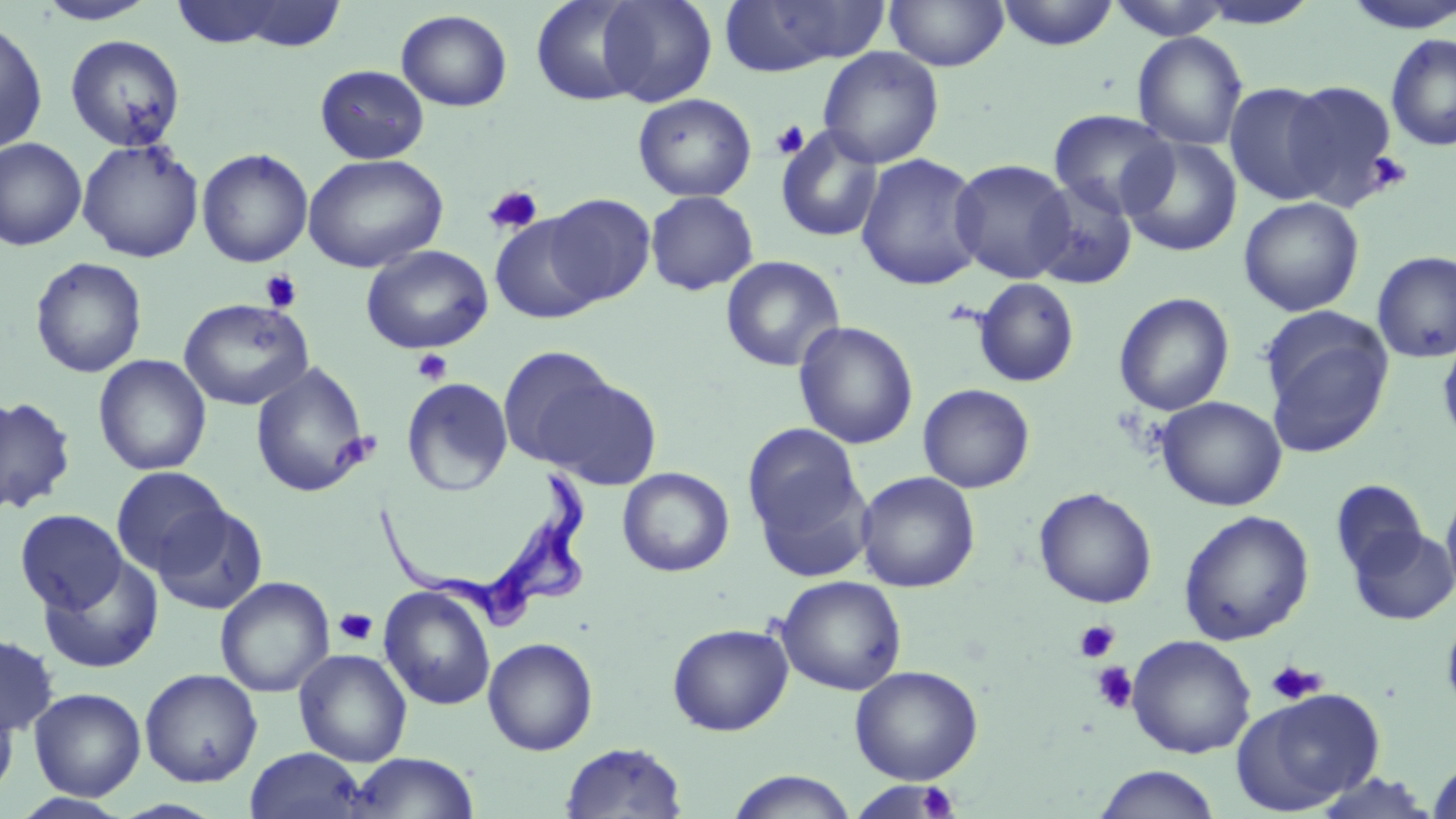
Summary:
  - Coordinate format: approximate bounding boxes as named x1/y1/x2/y2 corners in pixels
  - Uninfected red blood cell locations: (x1=164, y1=0, x2=323, y2=50), (x1=530, y1=0, x2=649, y2=106), (x1=597, y1=0, x2=717, y2=107), (x1=884, y1=0, x2=1009, y2=71), (x1=996, y1=0, x2=1119, y2=50), (x1=34, y1=1, x2=159, y2=25), (x1=719, y1=1, x2=888, y2=75), (x1=1104, y1=1, x2=1237, y2=40), (x1=1339, y1=1, x2=1456, y2=34), (x1=395, y1=9, x2=512, y2=112), (x1=0, y1=18, x2=48, y2=155), (x1=1132, y1=32, x2=1248, y2=151), (x1=1385, y1=33, x2=1456, y2=152), (x1=64, y1=34, x2=186, y2=152), (x1=817, y1=47, x2=944, y2=168), (x1=315, y1=64, x2=429, y2=164), (x1=1280, y1=80, x2=1401, y2=206), (x1=1224, y1=82, x2=1336, y2=205), (x1=633, y1=93, x2=757, y2=202), (x1=1049, y1=109, x2=1177, y2=218), (x1=776, y1=126, x2=884, y2=242), (x1=0, y1=137, x2=87, y2=251), (x1=1120, y1=137, x2=1242, y2=257), (x1=77, y1=139, x2=204, y2=263), (x1=197, y1=148, x2=313, y2=267), (x1=303, y1=153, x2=448, y2=273), (x1=855, y1=153, x2=986, y2=291), (x1=950, y1=159, x2=1075, y2=283), (x1=1026, y1=178, x2=1138, y2=290), (x1=645, y1=190, x2=759, y2=296), (x1=543, y1=193, x2=656, y2=306), (x1=1238, y1=197, x2=1364, y2=317), (x1=491, y1=215, x2=603, y2=324), (x1=361, y1=245, x2=493, y2=354), (x1=1372, y1=251, x2=1456, y2=363), (x1=720, y1=255, x2=845, y2=373), (x1=30, y1=257, x2=147, y2=378), (x1=972, y1=278, x2=1080, y2=387), (x1=1114, y1=292, x2=1234, y2=416), (x1=179, y1=298, x2=313, y2=411), (x1=1261, y1=313, x2=1393, y2=457), (x1=793, y1=321, x2=919, y2=450), (x1=1437, y1=338, x2=1456, y2=449), (x1=496, y1=346, x2=620, y2=468), (x1=93, y1=354, x2=212, y2=476), (x1=250, y1=362, x2=371, y2=499), (x1=535, y1=373, x2=663, y2=490), (x1=402, y1=377, x2=513, y2=497), (x1=918, y1=383, x2=1035, y2=493), (x1=0, y1=395, x2=77, y2=516), (x1=1155, y1=396, x2=1287, y2=511), (x1=742, y1=422, x2=868, y2=555), (x1=110, y1=466, x2=231, y2=577), (x1=617, y1=467, x2=735, y2=577), (x1=856, y1=471, x2=981, y2=593), (x1=1330, y1=479, x2=1427, y2=578), (x1=1441, y1=483, x2=1456, y2=603), (x1=1034, y1=487, x2=1157, y2=608), (x1=153, y1=503, x2=268, y2=615), (x1=15, y1=509, x2=127, y2=613), (x1=1178, y1=509, x2=1315, y2=645), (x1=1348, y1=525, x2=1456, y2=626), (x1=39, y1=556, x2=164, y2=673), (x1=775, y1=575, x2=907, y2=696), (x1=215, y1=576, x2=335, y2=698), (x1=378, y1=586, x2=496, y2=711), (x1=1441, y1=606, x2=1456, y2=721), (x1=667, y1=622, x2=793, y2=736), (x1=0, y1=633, x2=59, y2=737), (x1=1127, y1=634, x2=1256, y2=759), (x1=482, y1=637, x2=599, y2=755), (x1=294, y1=648, x2=412, y2=766), (x1=849, y1=665, x2=984, y2=784), (x1=140, y1=668, x2=263, y2=787), (x1=29, y1=687, x2=146, y2=801), (x1=1232, y1=688, x2=1385, y2=814), (x1=0, y1=690, x2=19, y2=803), (x1=560, y1=741, x2=688, y2=818), (x1=244, y1=746, x2=368, y2=818), (x1=347, y1=752, x2=480, y2=818), (x1=1426, y1=759, x2=1456, y2=818), (x1=1093, y1=765, x2=1222, y2=819), (x1=725, y1=770, x2=858, y2=818), (x1=1307, y1=771, x2=1441, y2=817), (x1=846, y1=781, x2=963, y2=818), (x1=11, y1=792, x2=135, y2=818)
  - Trypanosoma brucei locations: (x1=372, y1=472, x2=592, y2=634)
  - Platelet locations: (x1=770, y1=120, x2=810, y2=160), (x1=1367, y1=151, x2=1412, y2=193), (x1=483, y1=184, x2=544, y2=235), (x1=260, y1=270, x2=303, y2=314), (x1=412, y1=348, x2=453, y2=386), (x1=333, y1=607, x2=378, y2=646), (x1=1073, y1=619, x2=1119, y2=663), (x1=1264, y1=660, x2=1325, y2=704), (x1=1091, y1=661, x2=1137, y2=713), (x1=916, y1=783, x2=960, y2=818)
  - Slide-level diagnosis: Trypanosoma brucei
  - Modality: optical microscopy
  - Stain: May-Grünwald-Giemsa
  - Magnification: 1000x
  - Field of view: one of a larger specimen
  - Preparation: thin blood film
  - Image size: 1456×819 pixels